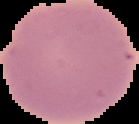
Summary:
  - Image size: 139×124 pixels
  - Image type: segmented cell region on a black background
  - Result: no malaria parasites detected
  - Preparation: thin blood film